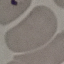
Summary:
  - Result: no malaria parasites detected
  - Stain: Giemsa
  - Preparation: thin blood smear
  - Image type: automatically extracted cell patch, resized to 64 × 64 pixels
  - Capture: smartphone camera at the microscope eyepiece